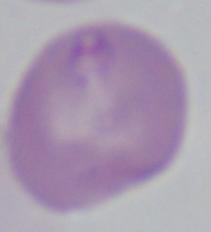
Summary:
  - Magnification: 1000x
  - Modality: micrograph
  - Identification: Babesia